State which parasite is depicted.
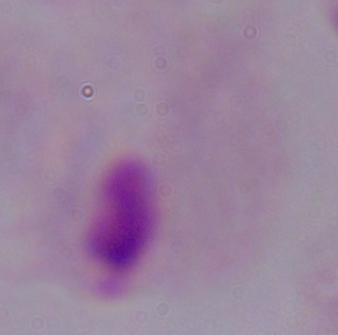

A trichomonad.

1000x magnification. Photomicrograph.